Assess the morphology of the red blood cells.
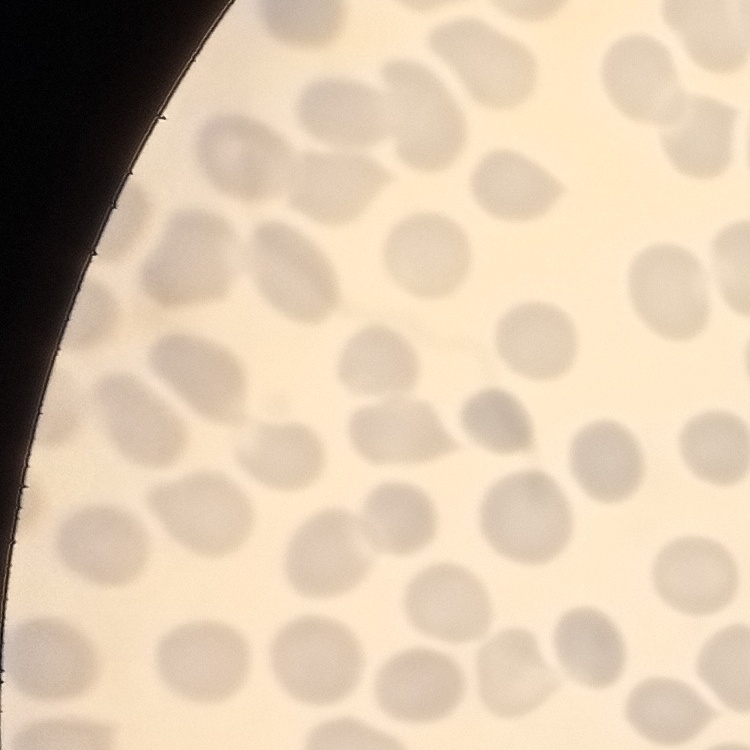
No rouleaux formation.

Square crop of a larger photomicrograph. Stained with either Field's or Giemsa. Thin peripheral smear.